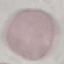 Result: no malaria parasites seen. Thin smear of blood. Cell patch, automatically extracted from a larger field of view and resized to 64 × 64 pixels. Giemsa stain. Acquired by smartphone through the microscope eyepiece.